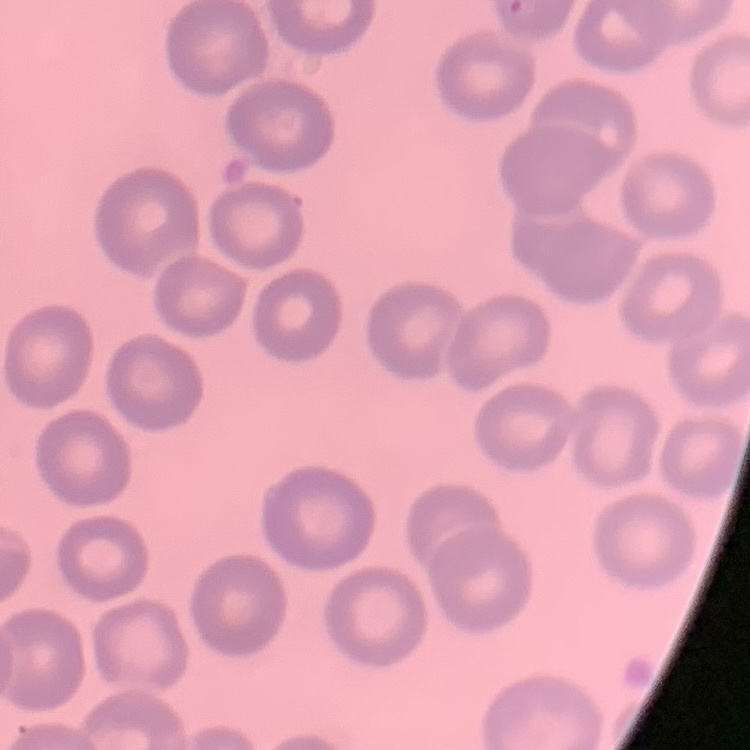

red blood cell morphology = no rouleaux formation
stain = Field's or Giemsa
image type = square crop of a larger photomicrograph
preparation = thin blood smear